Name the parasite shown.
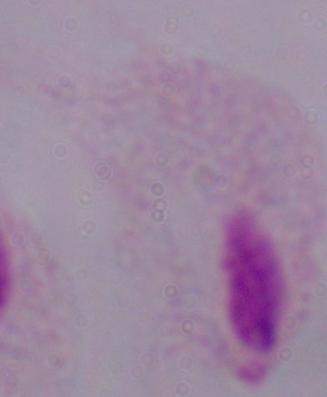

A trichomonad.

Captured at 1000x magnification. Micrograph.